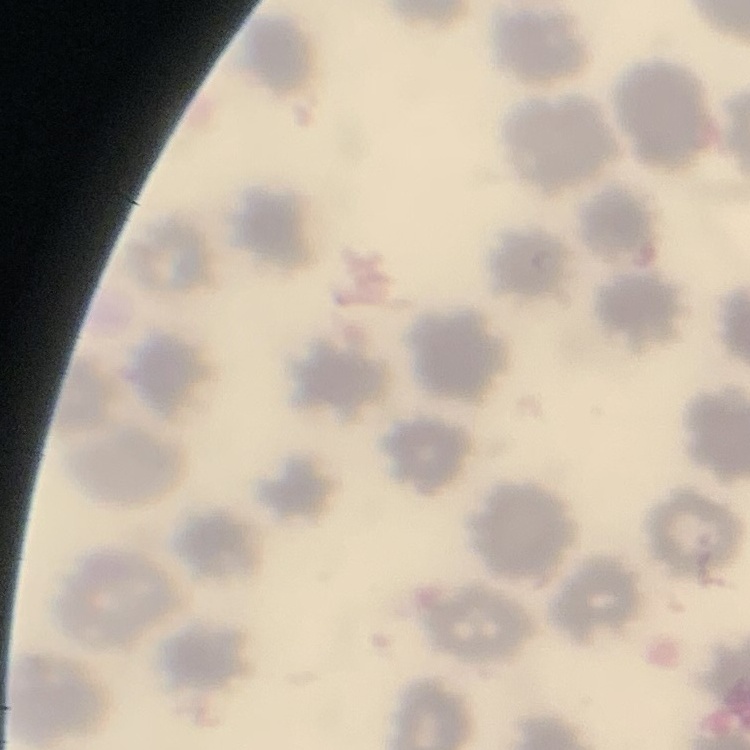

red blood cell morphology = no rouleaux formation
stain = Field's or Giemsa
preparation = thin blood film
image type = one tile cut from a larger photomicrograph